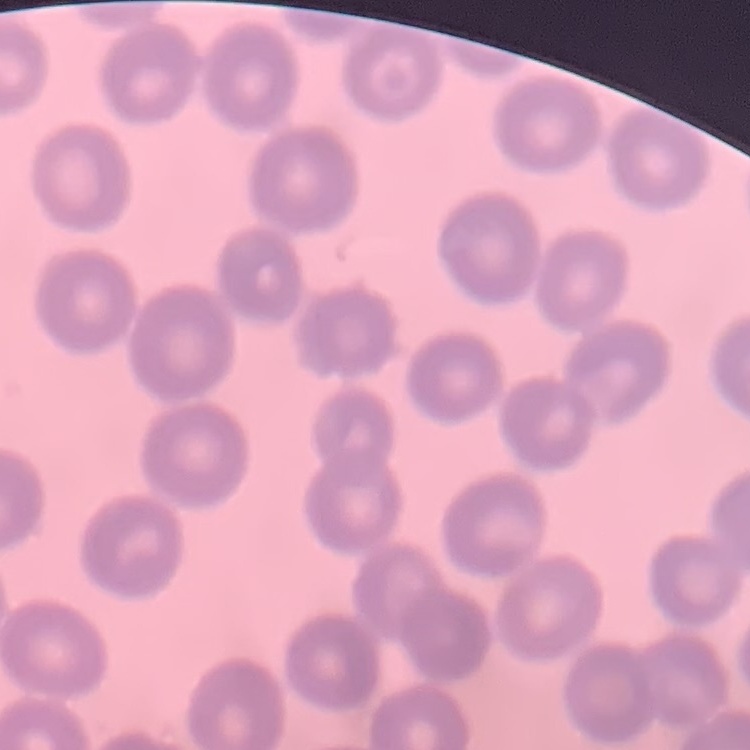

The erythrocytes exhibit no rouleaux formation. Thin blood smear. Stained with either Field's or Giemsa. One tile cut from a larger photomicrograph.